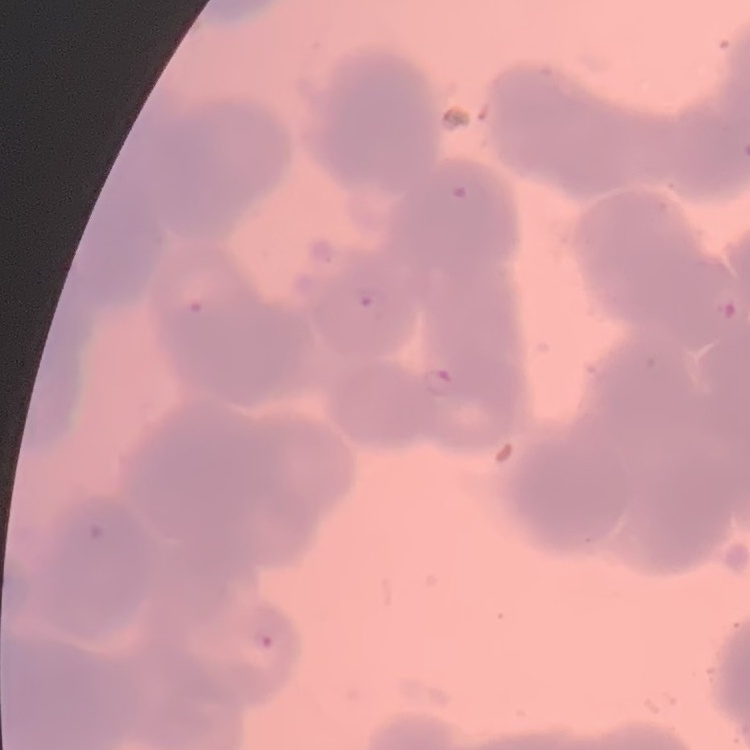

Summary:
  - Erythrocyte morphology: rouleaux formation
  - Image type: one tile cut from a larger photomicrograph
  - Preparation: thin blood smear
  - Stain: Field's or Giemsa